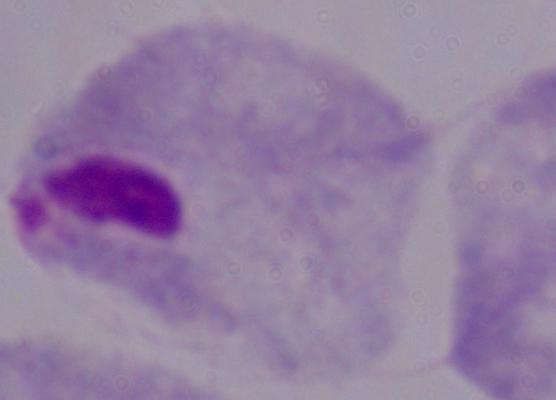

identification = trichomonad
magnification = 1000x
modality = micrograph